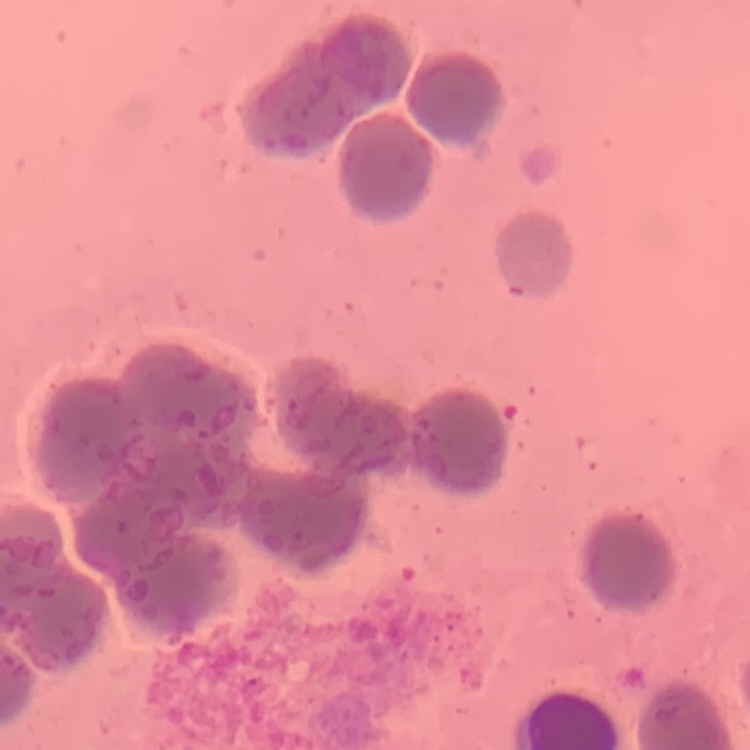 The red blood cells exhibit rouleaux formation. Square crop of a larger photomicrograph. Thin blood film. Field's or Giemsa stain.